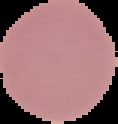

Result: no Plasmodium parasites detected. Image is 118×124 pixels. From a thin blood film. Segmented cell region on a black background.